Give the position of every leukocyte visible.
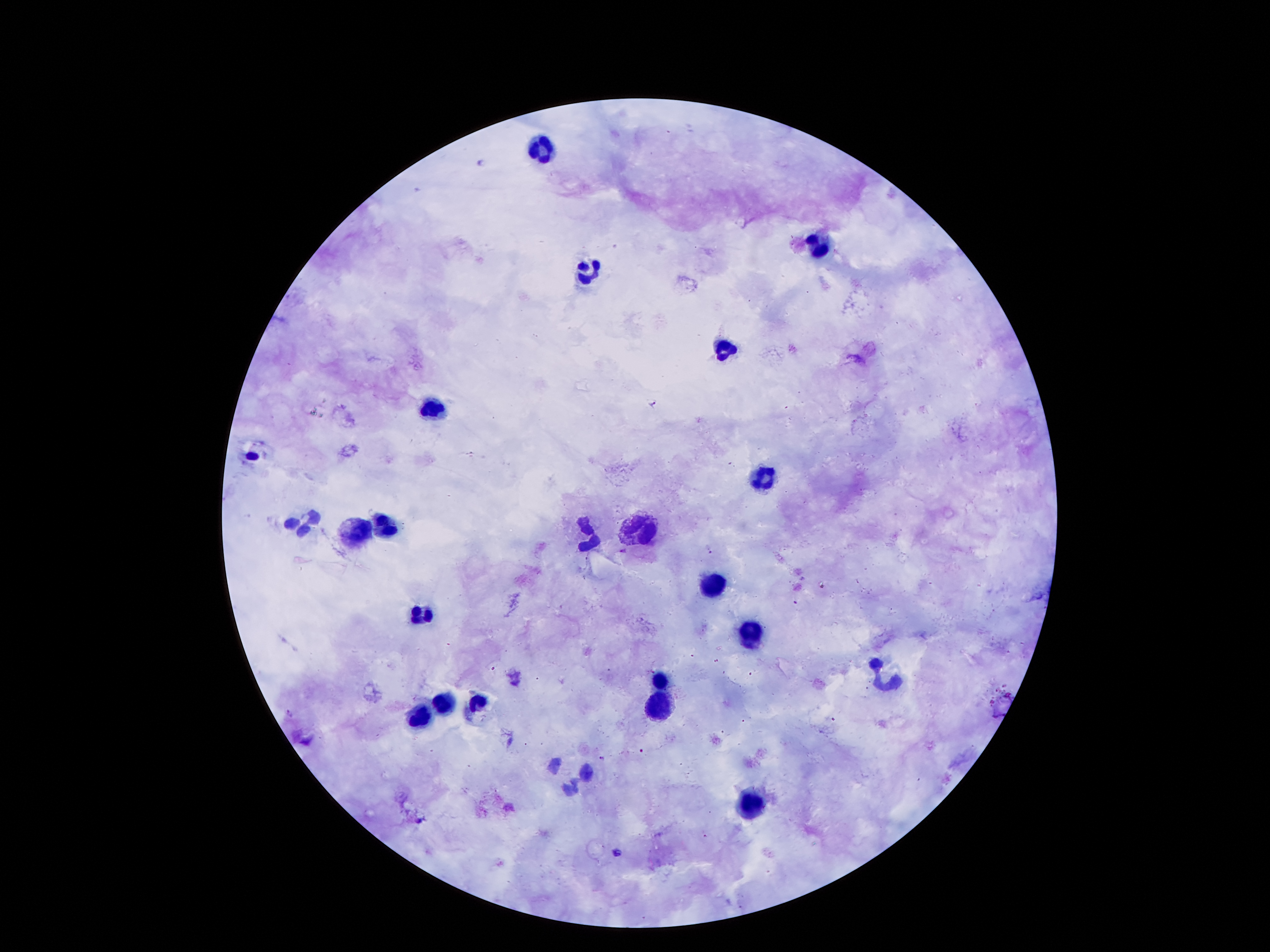

Approximate centers as [x, y] in pixels.
Leukocytes: [543, 156], [818, 249], [587, 273], [726, 349], [432, 405], [766, 475], [304, 522], [390, 525], [636, 529], [360, 532], [587, 532], [711, 580], [752, 634], [660, 677], [883, 684], [477, 699], [660, 703], [448, 705], [419, 719], [752, 806].

Summary:
  - Malaria parasite locations: [654, 403], [710, 549], [625, 550], [290, 713], [602, 759], [617, 852]
  - Patient malaria status: positive for Plasmodium falciparum
  - Preparation: thick blood smear
  - Image size: 1270×952 pixels
  - Stain: Giemsa
  - Capture: smartphone camera through the microscope eyepiece
  - Field of view: one from this slide
  - Magnification: 100x